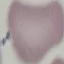

{
  "malaria_status": "uninfected",
  "image_type": "automatically extracted cell patch, resized to 64 × 64 pixels",
  "stain": "Giemsa",
  "capture": "smartphone camera at the microscope eyepiece",
  "preparation": "thin smear"
}